Give the extent of all Plasmodium falciparum-infected red blood cells.
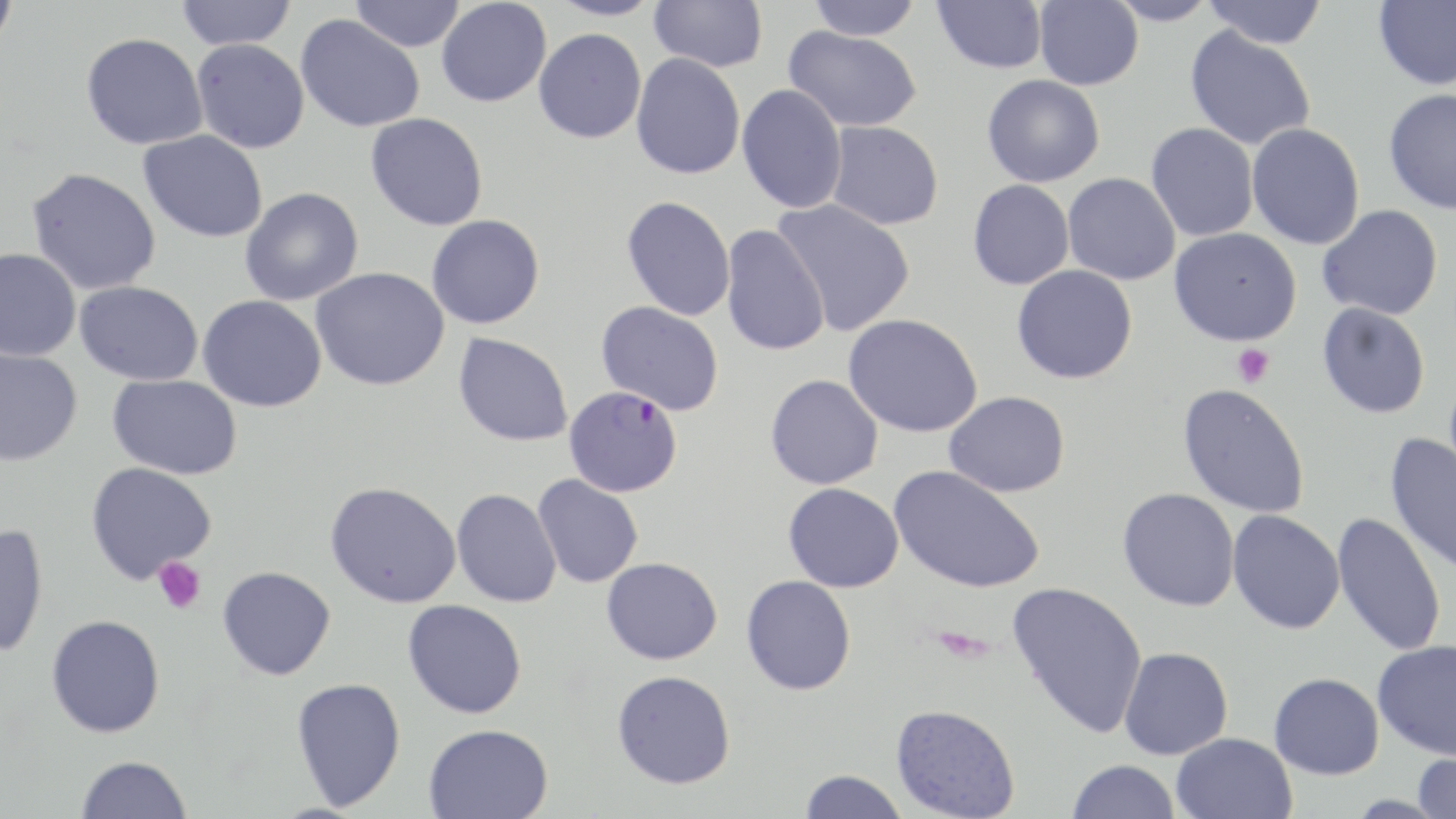

Approximate bounding boxes as (x1, y1, x2, y2) in pixels.
Plasmodium falciparum-infected red blood cells: (564, 386, 683, 497).

Platelet locations: (1232, 343, 1275, 388), (153, 557, 207, 615). Uninfected red blood cell locations: (0, 0, 19, 52), (175, 0, 296, 50), (349, 0, 465, 52), (436, 0, 551, 107), (547, 0, 665, 21), (649, 0, 768, 72), (805, 0, 923, 40), (932, 0, 1048, 74), (1034, 0, 1143, 90), (1106, 0, 1218, 26), (1201, 0, 1329, 49), (1373, 0, 1456, 90), (296, 14, 425, 132), (783, 25, 921, 132), (1184, 26, 1316, 150), (533, 28, 646, 143), (81, 32, 208, 150), (191, 37, 310, 153), (631, 53, 745, 180), (982, 74, 1105, 187), (737, 84, 847, 214), (1383, 88, 1456, 214), (365, 113, 488, 231), (826, 121, 944, 230), (1247, 122, 1365, 249), (1146, 123, 1259, 242), (138, 130, 268, 242), (26, 167, 162, 295), (1063, 173, 1181, 285), (967, 179, 1075, 290), (239, 187, 364, 306), (622, 196, 736, 321), (772, 199, 916, 337), (1317, 205, 1444, 320), (426, 215, 545, 329), (721, 224, 830, 356), (1169, 227, 1302, 346), (0, 248, 81, 361), (1011, 265, 1138, 384), (311, 267, 449, 390), (75, 281, 204, 386), (198, 295, 327, 412), (597, 302, 725, 415), (1317, 302, 1430, 418), (843, 313, 983, 438), (453, 332, 573, 447), (0, 348, 83, 466), (108, 374, 242, 480), (765, 374, 884, 489), (1177, 382, 1309, 519), (944, 391, 1070, 497), (1385, 432, 1456, 575), (85, 462, 217, 584), (889, 465, 1046, 593), (532, 474, 643, 589), (325, 481, 461, 608), (783, 482, 904, 592), (1117, 487, 1240, 611), (451, 488, 562, 608), (1227, 509, 1345, 634), (1331, 511, 1447, 657), (0, 523, 48, 659), (601, 557, 723, 665), (218, 566, 336, 680), (741, 575, 856, 696), (1007, 581, 1149, 738), (403, 599, 527, 718), (46, 614, 165, 738), (1372, 640, 1456, 760), (1118, 647, 1233, 760), (612, 670, 736, 789), (1269, 672, 1384, 779), (291, 677, 406, 810), (890, 704, 1020, 819), (423, 724, 553, 819), (1170, 732, 1298, 819), (1411, 751, 1456, 819), (76, 755, 192, 818), (1066, 759, 1181, 818), (798, 770, 909, 818). Slide-level diagnosis: Plasmodium falciparum. Image is 1456×819 pixels. Captured at 1000x magnification. Thin blood film. Optical microscopy. May-Grünwald-Giemsa-stained preparation. One field of a larger specimen.